State which parasite is depicted.
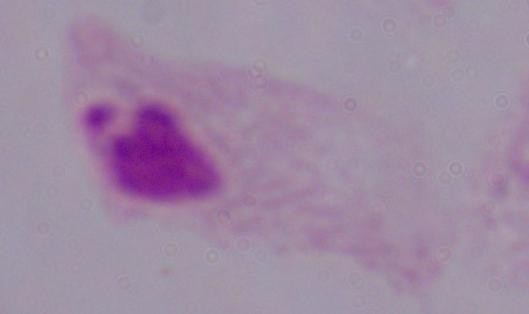

This is a trichomonad.

1000x magnification. Photomicrograph.